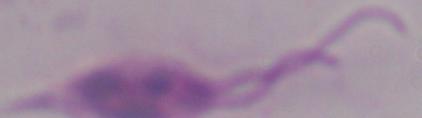
{
  "magnification": "1000x",
  "identification": "Leishmania",
  "modality": "photomicrograph"
}